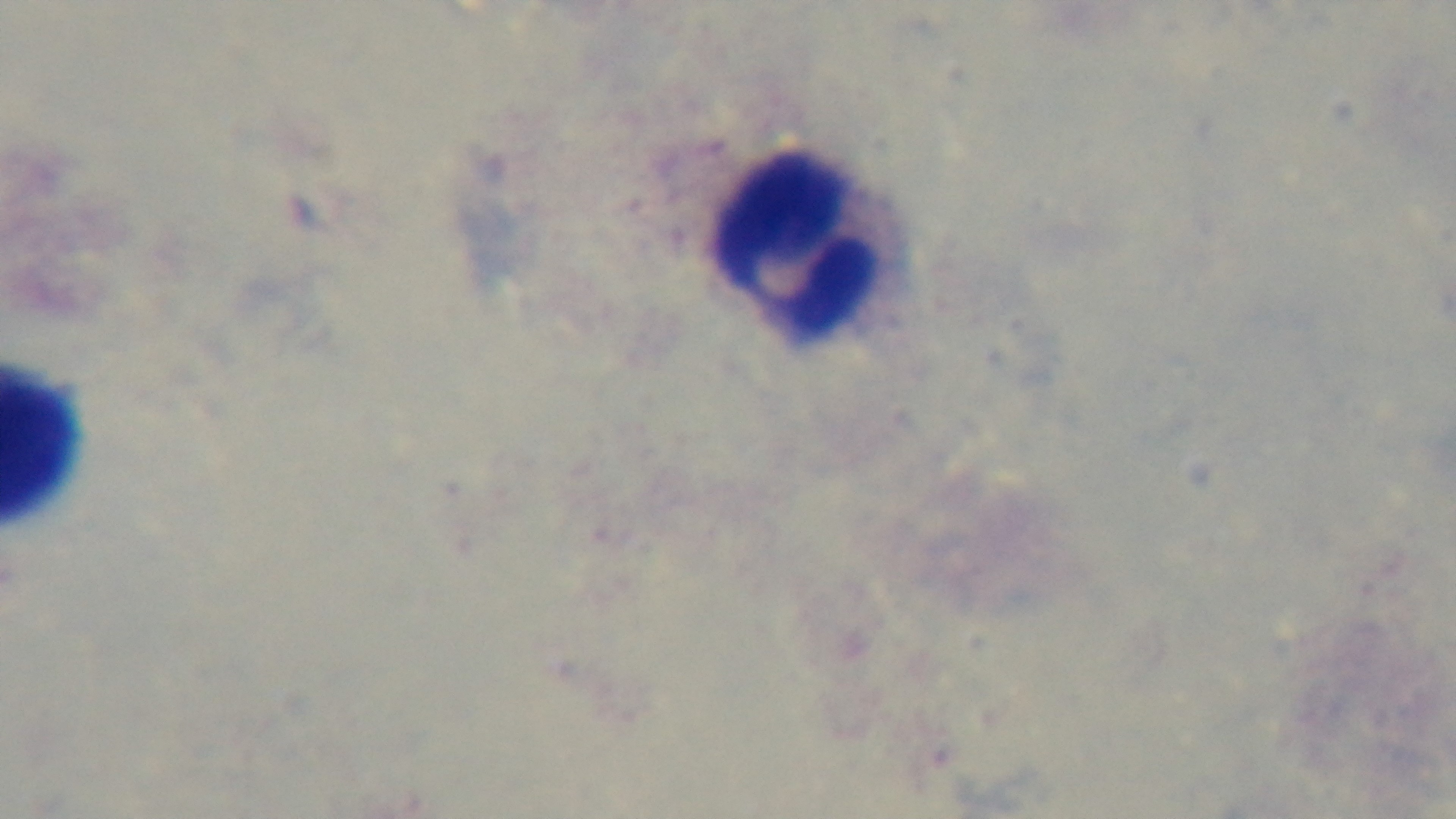
modality = light microscopy
preparation = thick blood film
malaria status = uninfected
stain = Giemsa
objective = 100x oil immersion
field of view = one from the slide
capture = mounted 4K digital camera